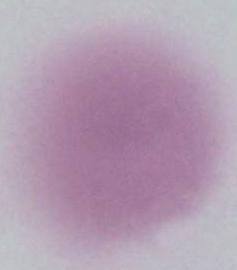

Summary:
  - Magnification: 1000x
  - Modality: photomicrograph
  - Identification: red blood cell